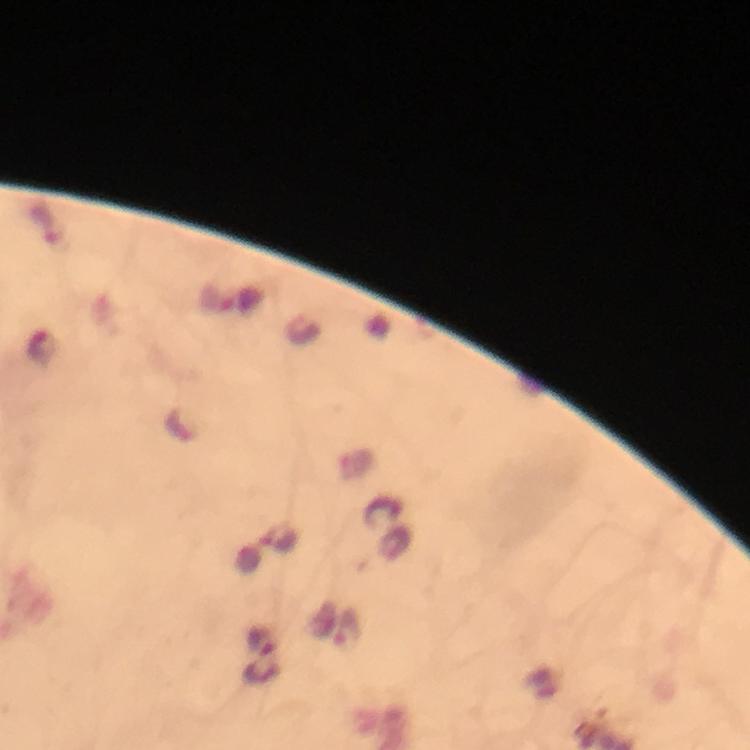

magnification = 100x
Plasmodium parasite locations = approximate centers as {x, y} in pixels: {41, 348}, {348, 630}
stain = Giemsa
context = from a malaria diagnostic workup
cropped from = one field of view
preparation = thick blood smear
immersion oil = applied
capture = smartphone camera through the microscope
image size = 750×750 pixels